Name the parasite shown.
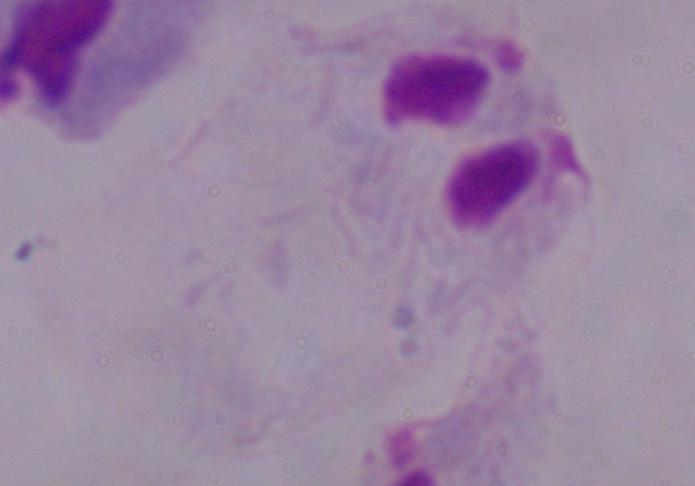

A trichomonad.

Micrograph. 1000x magnification.